Give the position of every Plasmodium parasite visible.
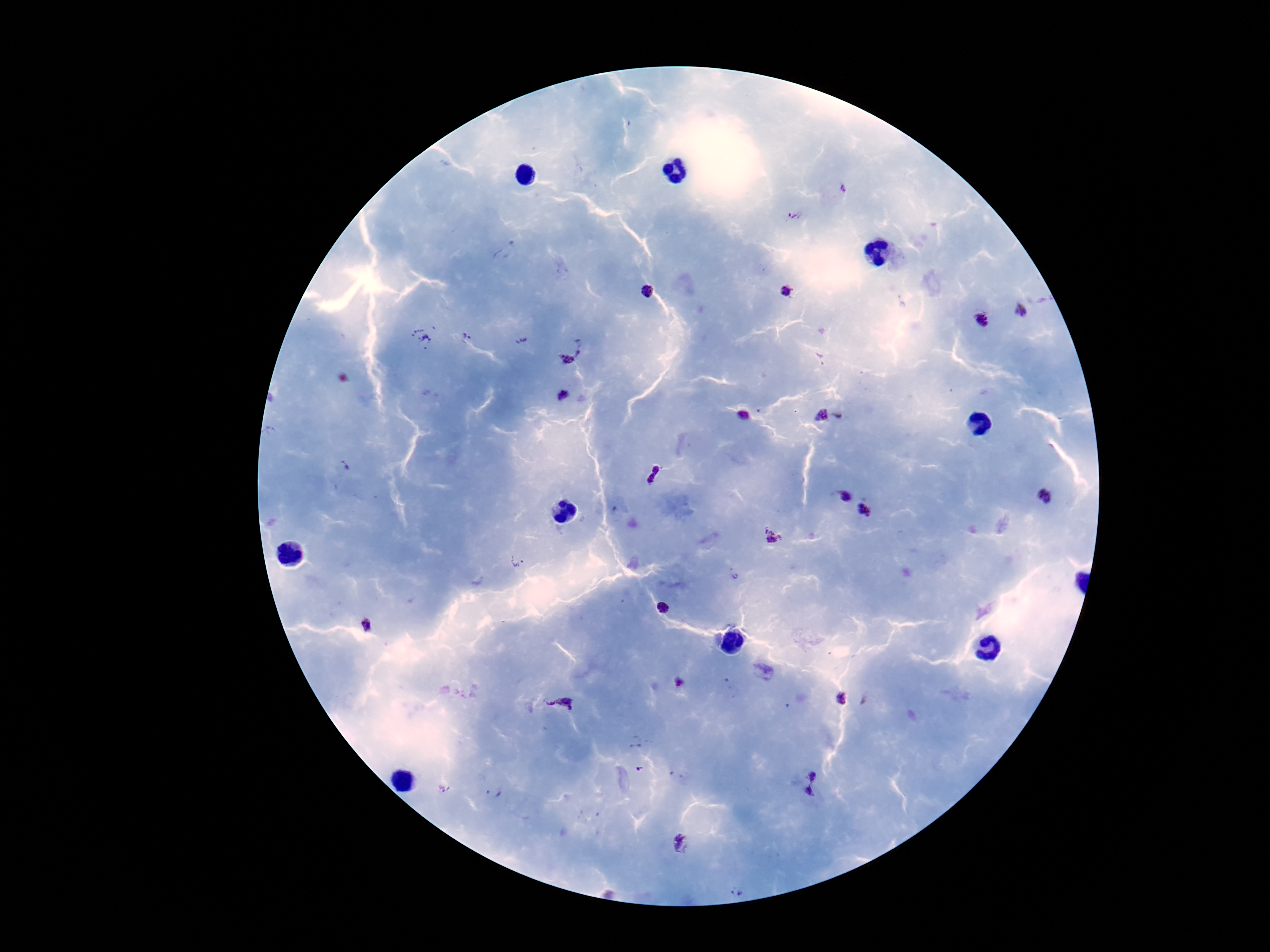

Approximate centers as (x, y) in pixels.
Plasmodium parasites: (842, 188), (795, 216), (648, 291), (785, 292), (1021, 309), (982, 319), (467, 335), (421, 338), (522, 341), (580, 346), (566, 361), (562, 395), (742, 416), (821, 416), (345, 465), (654, 474), (844, 497), (1046, 497), (865, 511), (775, 535), (518, 561), (663, 609), (367, 626), (841, 698), (560, 703), (639, 769), (812, 775), (493, 794), (809, 796), (683, 844), (738, 891).

Patient malaria status: infected. Smartphone photograph taken through the microscope eyepiece. 100x magnification. Image is 1270×952 pixels. Thick blood film. Giemsa-stained preparation. One field from this slide.